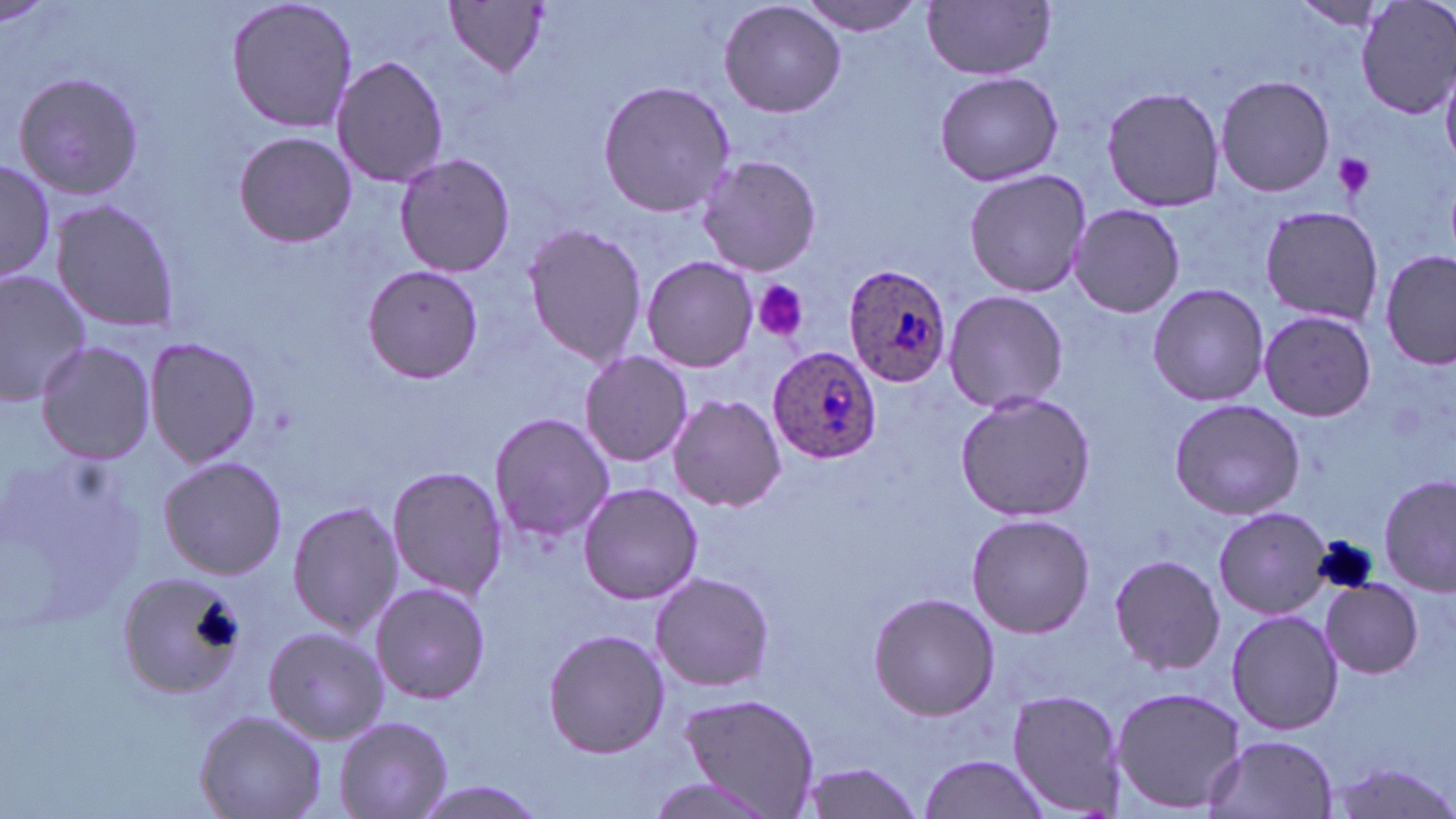
Approximate bounding boxes as (x1,y1)-(x2,y2) corner pairs in pixels. Plasmodium ovale-infected red blood cell locations: (842,262)-(953,389), (767,345)-(883,462). Platelet locations: (1331,152)-(1377,200), (753,280)-(810,343). Uninfected red blood cell locations: (225,0)-(358,134), (719,0)-(845,118), (797,0)-(927,37), (1357,0)-(1456,119), (1287,1)-(1393,33), (444,2)-(552,82), (924,2)-(1055,80), (332,56)-(448,189), (1442,66)-(1456,172), (9,70)-(149,200), (933,70)-(1065,186), (1216,73)-(1335,198), (596,79)-(736,216), (1101,84)-(1226,212), (234,132)-(356,246), (393,152)-(516,279), (697,153)-(821,279), (0,159)-(58,287), (964,168)-(1094,297), (48,197)-(183,334), (1257,203)-(1386,325), (1065,204)-(1185,317), (522,223)-(648,368), (1381,251)-(1455,370), (641,255)-(760,373), (360,264)-(485,385), (0,266)-(93,402), (1146,283)-(1271,407), (943,288)-(1068,415), (1257,308)-(1377,422), (143,336)-(263,470), (35,341)-(157,463), (579,351)-(693,466), (954,389)-(1098,521), (667,394)-(786,512), (1170,398)-(1306,520), (489,413)-(617,540), (4,443)-(147,632), (158,456)-(289,579), (387,463)-(512,599), (1380,473)-(1454,598), (577,481)-(704,606), (285,497)-(403,639), (1213,506)-(1333,619), (964,514)-(1095,639), (1109,553)-(1225,675), (649,571)-(775,692), (120,573)-(247,697), (1319,579)-(1425,678), (370,580)-(490,705), (866,591)-(999,721), (1226,608)-(1345,735), (263,626)-(387,746), (542,628)-(670,758), (1110,686)-(1249,813), (1009,689)-(1127,814), (675,691)-(821,815), (194,709)-(327,819), (335,716)-(452,817), (1203,734)-(1338,819), (917,753)-(1054,819), (799,758)-(926,819), (1324,760)-(1456,819), (638,775)-(779,819), (404,779)-(553,817). Slide-level diagnosis: Plasmodium ovale. Image is 1456×819 pixels. Optical microscopy. Thin blood smear. Single field of view. May-Grünwald-Giemsa stain. Captured at 1000x magnification.